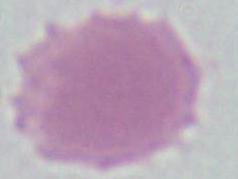
Summary:
  - Modality: micrograph
  - Magnification: 1000x
  - Identification: red blood cell